Evaluate for Plasmodium parasites.
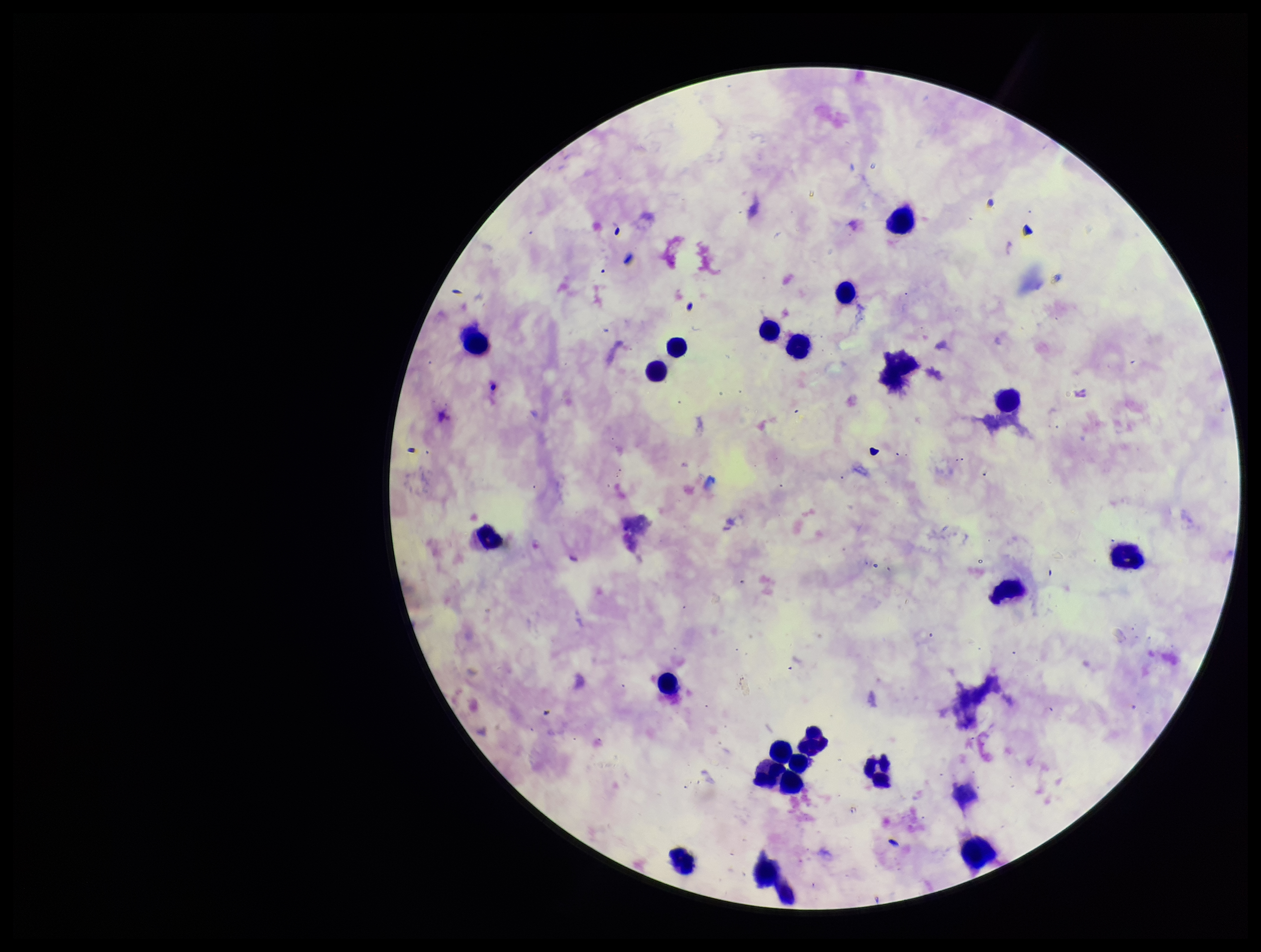
None identified.

Species reported for this patient: Plasmodium falciparum. Parasite count: 0. Giemsa stain. Preparation: thick blood smear. One field from this slide. Photographed through the microscope eyepiece with a smartphone camera. Leukocyte count: 23. Patient malaria status: positive. Image is 1261×952 pixels.